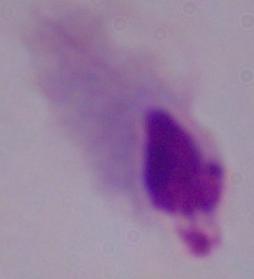
modality = micrograph
identification = trichomonad
magnification = 1000x